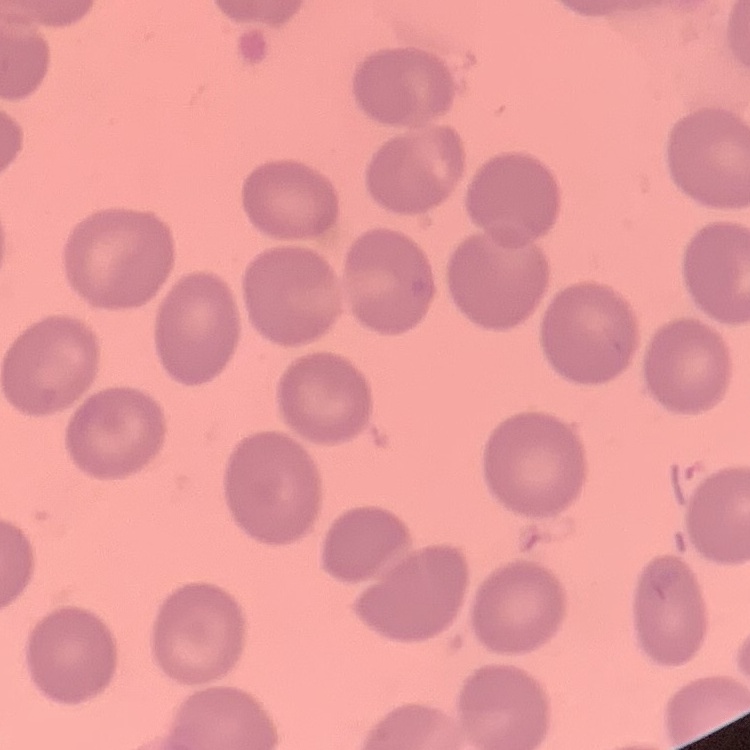
The erythrocytes show no rouleaux formation. One tile cut from a larger photomicrograph. Thin blood film. Stained with either Field's or Giemsa.